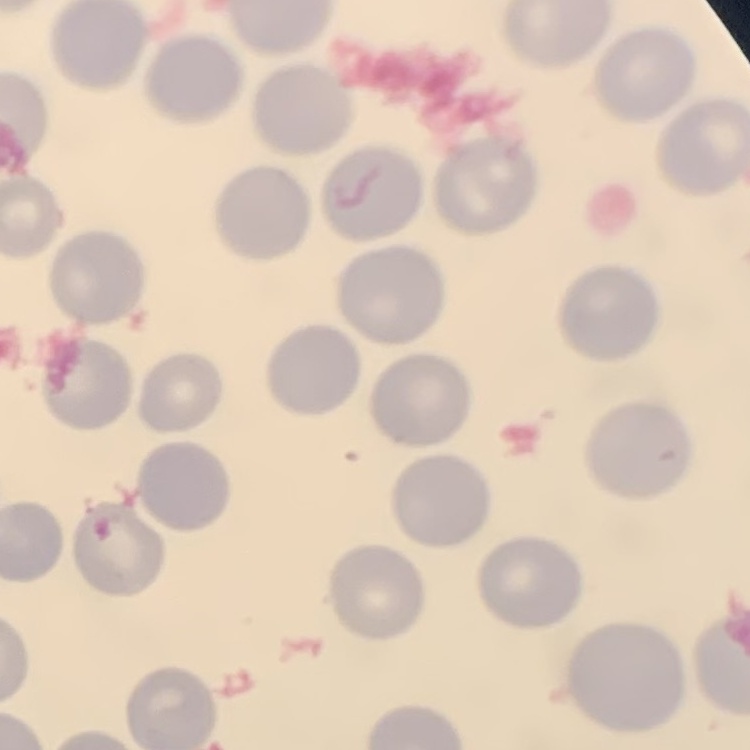
Summary:
  - Erythrocyte morphology: no rouleaux formation
  - Stain: Field's or Giemsa
  - Preparation: thin blood film
  - Image type: square crop of a larger photomicrograph